Classify this cell by malaria status.
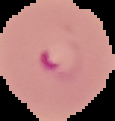

Parasitized.

The area outside the segmented cell region is set to black. Image is 115×121 pixels. From a thin blood film.